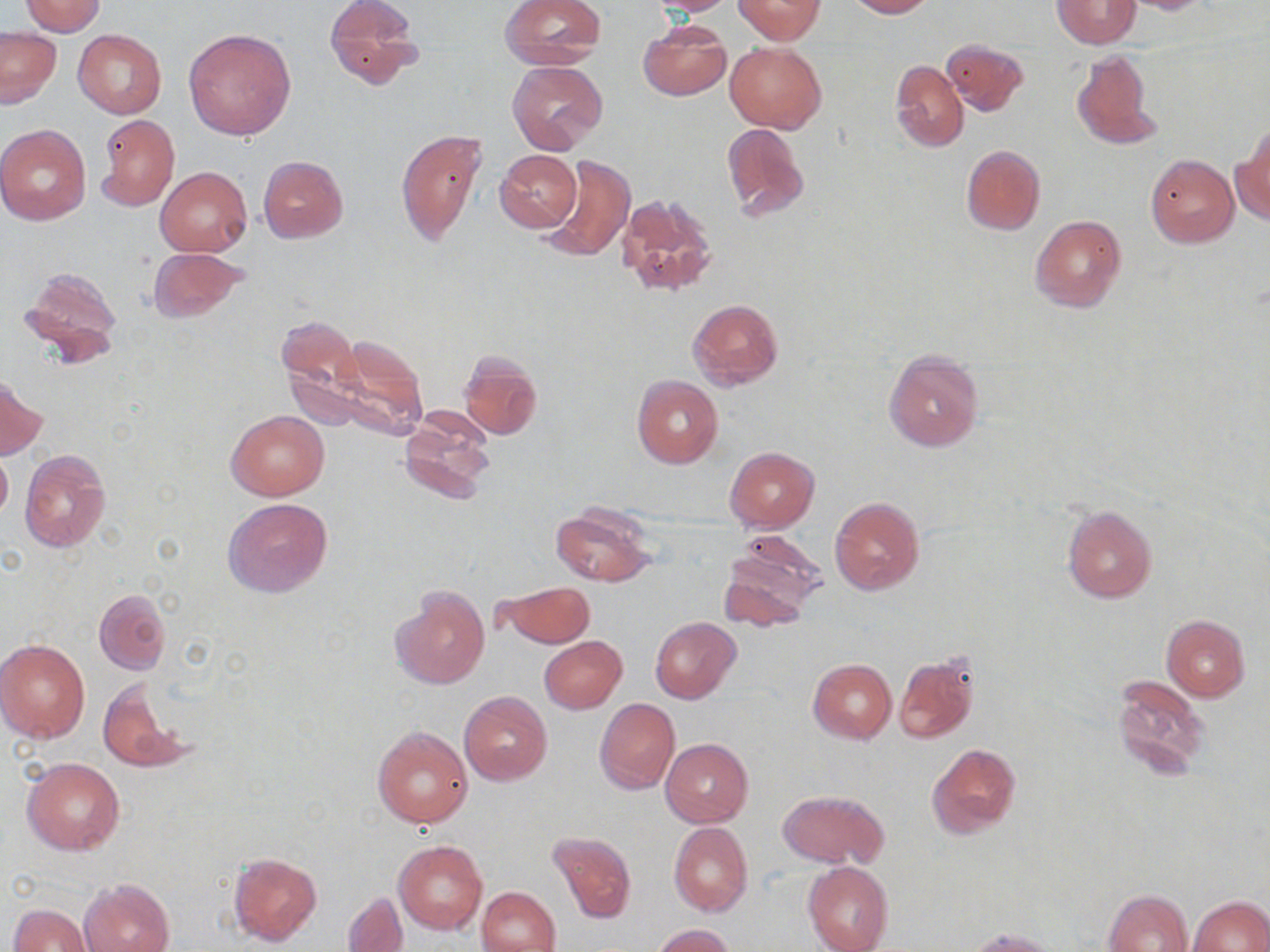
slide_level_diagnosis: no evidence of blood parasites
field_of_view: one of a larger specimen
uninfected_red_blood_cell_locations: 'approximate bounding boxes as named x1/y1/x2/y2 corners in pixels: (x1=323, y1=0, x2=422, y2=89), (x1=500, y1=0, x2=605, y2=68), (x1=646, y1=0, x2=740, y2=15), (x1=734, y1=0, x2=824, y2=42), (x1=847, y1=0, x2=932, y2=18), (x1=1053, y1=0, x2=1141, y2=48), (x1=1119, y1=0, x2=1213, y2=14), (x1=21, y1=1, x2=106, y2=36), (x1=638, y1=22, x2=731, y2=101), (x1=0, y1=28, x2=61, y2=108), (x1=184, y1=28, x2=296, y2=141), (x1=73, y1=29, x2=168, y2=119), (x1=942, y1=39, x2=1028, y2=115), (x1=725, y1=42, x2=826, y2=135), (x1=1071, y1=48, x2=1161, y2=149), (x1=890, y1=59, x2=969, y2=151), (x1=509, y1=60, x2=608, y2=155), (x1=96, y1=114, x2=179, y2=210), (x1=721, y1=122, x2=811, y2=223), (x1=0, y1=124, x2=91, y2=225), (x1=397, y1=128, x2=488, y2=246), (x1=1234, y1=131, x2=1270, y2=224), (x1=961, y1=144, x2=1045, y2=235), (x1=495, y1=149, x2=582, y2=233), (x1=541, y1=154, x2=635, y2=263), (x1=1147, y1=154, x2=1239, y2=247), (x1=258, y1=155, x2=350, y2=243), (x1=156, y1=167, x2=251, y2=257), (x1=617, y1=193, x2=719, y2=299), (x1=1030, y1=215, x2=1126, y2=314), (x1=147, y1=247, x2=249, y2=322), (x1=18, y1=266, x2=123, y2=368), (x1=687, y1=299, x2=784, y2=391), (x1=276, y1=318, x2=374, y2=430), (x1=330, y1=334, x2=429, y2=436), (x1=882, y1=350, x2=984, y2=452), (x1=458, y1=352, x2=542, y2=440), (x1=633, y1=375, x2=723, y2=469), (x1=0, y1=376, x2=46, y2=458), (x1=399, y1=408, x2=496, y2=503), (x1=227, y1=410, x2=329, y2=500), (x1=724, y1=447, x2=819, y2=532), (x1=0, y1=448, x2=12, y2=524), (x1=19, y1=449, x2=112, y2=553), (x1=830, y1=496, x2=925, y2=596), (x1=223, y1=497, x2=334, y2=599), (x1=1061, y1=504, x2=1157, y2=603), (x1=550, y1=506, x2=658, y2=586), (x1=719, y1=547, x2=819, y2=630), (x1=497, y1=581, x2=595, y2=648), (x1=389, y1=584, x2=490, y2=692), (x1=94, y1=589, x2=171, y2=674), (x1=1161, y1=615, x2=1251, y2=701), (x1=650, y1=617, x2=741, y2=703), (x1=539, y1=636, x2=627, y2=714), (x1=0, y1=640, x2=91, y2=743), (x1=894, y1=653, x2=979, y2=744), (x1=808, y1=660, x2=897, y2=743), (x1=1111, y1=675, x2=1211, y2=781), (x1=98, y1=680, x2=191, y2=775), (x1=459, y1=690, x2=553, y2=786), (x1=595, y1=698, x2=680, y2=794), (x1=372, y1=727, x2=472, y2=827), (x1=661, y1=738, x2=753, y2=827), (x1=928, y1=743, x2=1021, y2=839), (x1=22, y1=758, x2=125, y2=854), (x1=779, y1=790, x2=889, y2=868), (x1=669, y1=822, x2=753, y2=916), (x1=548, y1=830, x2=636, y2=924), (x1=394, y1=840, x2=487, y2=933), (x1=228, y1=851, x2=322, y2=947), (x1=803, y1=860, x2=894, y2=952), (x1=80, y1=877, x2=174, y2=952), (x1=477, y1=887, x2=561, y2=952), (x1=1104, y1=889, x2=1193, y2=952), (x1=343, y1=892, x2=408, y2=951), (x1=1190, y1=895, x2=1269, y2=952), (x1=9, y1=903, x2=94, y2=951), (x1=654, y1=925, x2=737, y2=951), (x1=964, y1=928, x2=1058, y2=952)'
preparation: thin blood film
image_size: 1270×952 pixels
modality: optical microscopy
stain: May-Grünwald-Giemsa
magnification: 1000x